Report the malaria status of this cell.
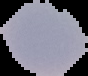
Uninfected.

Cell region segmented out of the field of view; the surrounding area is masked to black. From a thin blood film. Image is 88×76 pixels.